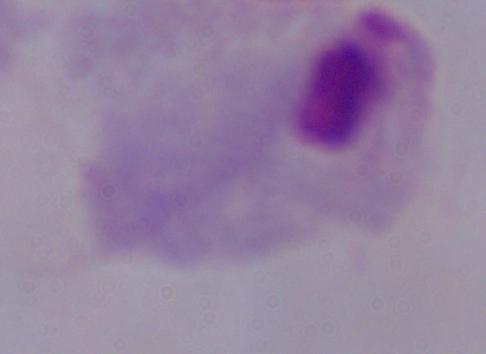
Micrograph. A trichomonad is seen. 1000x magnification.